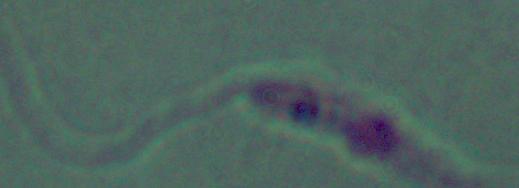

Summary:
  - Modality: photomicrograph
  - Identification: Leishmania
  - Magnification: 1000x